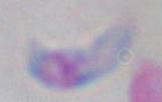

identification: Toxoplasma gondii
modality: micrograph
magnification: 1000x